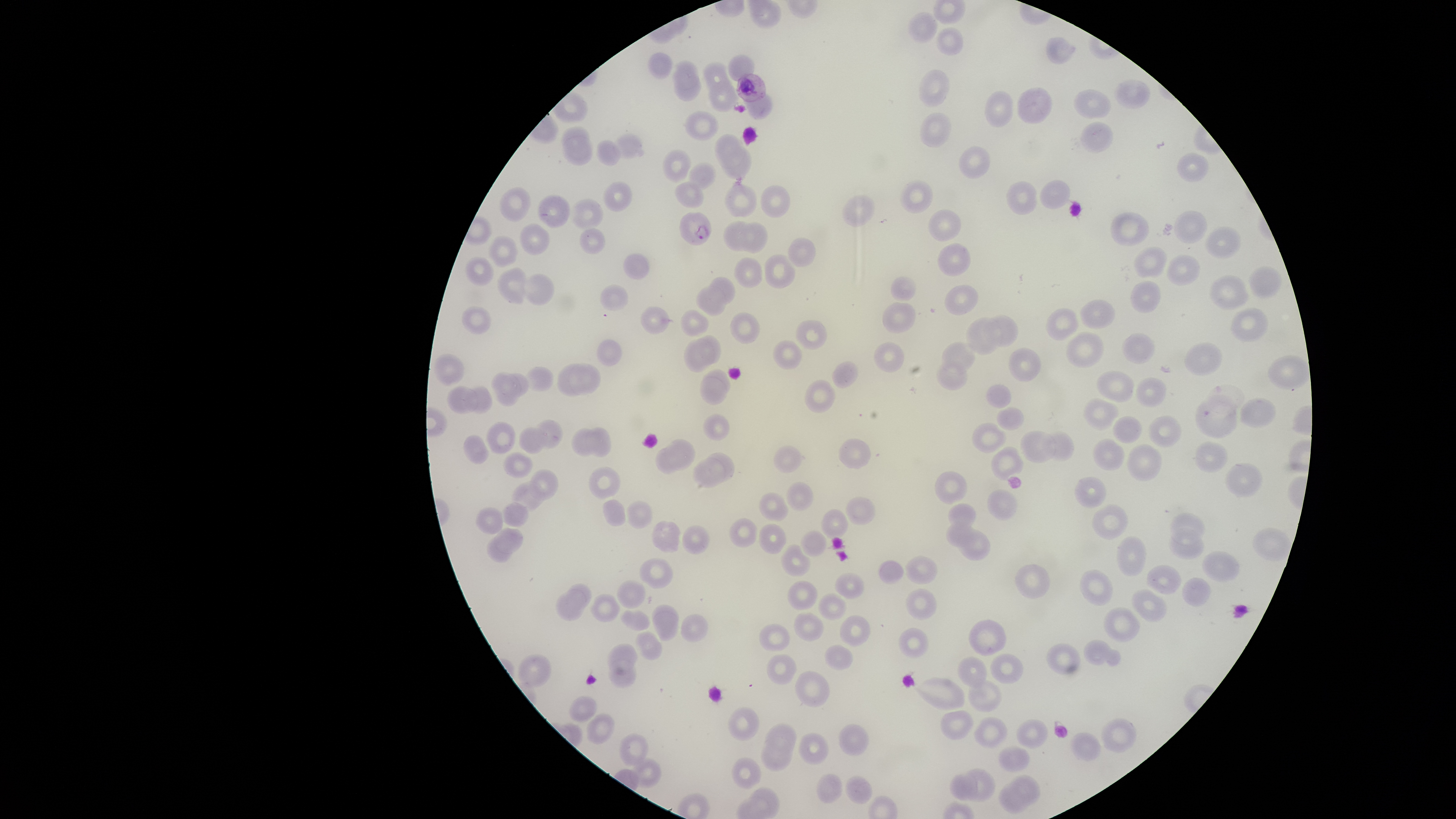
Approximate bounding boxes, in pixels from the top-left corner.
Summary:
  - Parasitized RBCs: (left=736, top=73, right=766, bottom=102), (left=679, top=211, right=712, bottom=246)
  - Uninfected RBCs: (left=747, top=0, right=782, bottom=28), (left=908, top=12, right=939, bottom=43), (left=935, top=26, right=964, bottom=55), (left=1045, top=36, right=1077, bottom=64), (left=648, top=52, right=672, bottom=80), (left=728, top=54, right=755, bottom=81), (left=672, top=59, right=702, bottom=89), (left=703, top=61, right=732, bottom=89), (left=919, top=69, right=950, bottom=109), (left=673, top=75, right=703, bottom=101), (left=707, top=80, right=740, bottom=113), (left=1113, top=80, right=1151, bottom=108), (left=1017, top=87, right=1052, bottom=124), (left=1073, top=89, right=1113, bottom=119), (left=984, top=90, right=1014, bottom=128), (left=743, top=94, right=772, bottom=120), (left=683, top=110, right=720, bottom=141), (left=920, top=112, right=952, bottom=149), (left=1080, top=121, right=1113, bottom=154), (left=562, top=125, right=588, bottom=149), (left=613, top=133, right=645, bottom=159), (left=715, top=133, right=746, bottom=166), (left=563, top=136, right=593, bottom=165), (left=596, top=139, right=621, bottom=166), (left=958, top=145, right=991, bottom=180), (left=721, top=147, right=751, bottom=181), (left=662, top=149, right=692, bottom=183), (left=1176, top=152, right=1210, bottom=182), (left=689, top=162, right=715, bottom=192), (left=899, top=180, right=934, bottom=214), (left=1006, top=180, right=1038, bottom=215), (left=1039, top=180, right=1071, bottom=210), (left=603, top=181, right=632, bottom=211), (left=675, top=181, right=704, bottom=208), (left=725, top=185, right=757, bottom=218), (left=760, top=185, right=791, bottom=218), (left=499, top=186, right=532, bottom=223), (left=536, top=195, right=570, bottom=229), (left=841, top=195, right=875, bottom=228), (left=570, top=199, right=604, bottom=230), (left=928, top=209, right=961, bottom=242), (left=1173, top=210, right=1208, bottom=245), (left=1110, top=212, right=1150, bottom=246), (left=723, top=219, right=758, bottom=252), (left=740, top=222, right=768, bottom=254), (left=520, top=223, right=550, bottom=256), (left=1205, top=226, right=1242, bottom=259), (left=580, top=228, right=605, bottom=255), (left=488, top=236, right=517, bottom=266), (left=788, top=237, right=816, bottom=268), (left=937, top=243, right=971, bottom=276), (left=1133, top=246, right=1169, bottom=278), (left=623, top=252, right=651, bottom=280), (left=763, top=253, right=795, bottom=289), (left=1165, top=255, right=1201, bottom=286), (left=465, top=256, right=495, bottom=285), (left=733, top=256, right=763, bottom=288), (left=1249, top=266, right=1282, bottom=297), (left=497, top=267, right=526, bottom=305), (left=525, top=273, right=555, bottom=306), (left=1209, top=275, right=1250, bottom=310), (left=709, top=276, right=736, bottom=305), (left=891, top=276, right=917, bottom=301), (left=1130, top=280, right=1161, bottom=314), (left=600, top=284, right=629, bottom=312), (left=944, top=285, right=978, bottom=315), (left=695, top=286, right=727, bottom=317), (left=1079, top=298, right=1116, bottom=329), (left=881, top=301, right=916, bottom=334), (left=462, top=305, right=492, bottom=334), (left=641, top=306, right=671, bottom=334), (left=1046, top=307, right=1080, bottom=341), (left=1230, top=307, right=1268, bottom=340), (left=680, top=308, right=709, bottom=338), (left=729, top=312, right=761, bottom=344), (left=983, top=314, right=1019, bottom=347), (left=965, top=316, right=1003, bottom=355), (left=795, top=320, right=828, bottom=349), (left=1066, top=331, right=1105, bottom=369), (left=1122, top=332, right=1156, bottom=364), (left=695, top=335, right=721, bottom=365), (left=596, top=339, right=623, bottom=366), (left=684, top=339, right=714, bottom=373), (left=772, top=340, right=802, bottom=369), (left=873, top=341, right=905, bottom=372), (left=942, top=342, right=975, bottom=373), (left=1184, top=342, right=1223, bottom=376), (left=1007, top=347, right=1042, bottom=382), (left=434, top=353, right=464, bottom=386), (left=831, top=360, right=859, bottom=389), (left=568, top=361, right=601, bottom=395), (left=935, top=361, right=968, bottom=390), (left=558, top=362, right=587, bottom=397), (left=525, top=366, right=554, bottom=392), (left=703, top=369, right=730, bottom=396), (left=491, top=371, right=521, bottom=406), (left=1097, top=371, right=1135, bottom=402), (left=507, top=372, right=529, bottom=396), (left=700, top=377, right=727, bottom=405), (left=1135, top=377, right=1167, bottom=407), (left=804, top=379, right=837, bottom=414), (left=987, top=384, right=1012, bottom=409), (left=447, top=385, right=479, bottom=414), (left=464, top=386, right=493, bottom=414), (left=1083, top=398, right=1120, bottom=431), (left=1240, top=398, right=1276, bottom=428), (left=1196, top=400, right=1239, bottom=439), (left=996, top=407, right=1025, bottom=431), (left=703, top=414, right=730, bottom=441), (left=1148, top=415, right=1182, bottom=448), (left=1113, top=416, right=1142, bottom=443), (left=534, top=419, right=563, bottom=448), (left=486, top=421, right=517, bottom=454), (left=972, top=421, right=1006, bottom=454), (left=518, top=426, right=547, bottom=455), (left=588, top=426, right=611, bottom=458), (left=571, top=427, right=599, bottom=457), (left=1020, top=431, right=1057, bottom=464), (left=1043, top=431, right=1075, bottom=461), (left=464, top=434, right=489, bottom=463), (left=666, top=438, right=696, bottom=470), (left=838, top=438, right=871, bottom=469), (left=1093, top=438, right=1125, bottom=471), (left=1195, top=441, right=1228, bottom=472), (left=1127, top=444, right=1162, bottom=481), (left=774, top=445, right=803, bottom=473), (left=656, top=446, right=682, bottom=475), (left=991, top=446, right=1024, bottom=481), (left=503, top=451, right=533, bottom=478), (left=704, top=453, right=735, bottom=482), (left=691, top=461, right=721, bottom=488), (left=1224, top=462, right=1263, bottom=497), (left=588, top=466, right=622, bottom=499), (left=528, top=468, right=559, bottom=500), (left=934, top=471, right=968, bottom=505), (left=1075, top=477, right=1106, bottom=509), (left=511, top=481, right=544, bottom=513), (left=786, top=482, right=814, bottom=511), (left=987, top=489, right=1018, bottom=521), (left=759, top=492, right=790, bottom=522), (left=845, top=496, right=877, bottom=525), (left=603, top=499, right=627, bottom=527), (left=626, top=500, right=654, bottom=530), (left=502, top=503, right=528, bottom=527), (left=948, top=503, right=977, bottom=530), (left=1093, top=503, right=1129, bottom=540), (left=476, top=507, right=503, bottom=535), (left=820, top=509, right=849, bottom=539), (left=1170, top=511, right=1205, bottom=546), (left=729, top=518, right=758, bottom=547), (left=652, top=520, right=683, bottom=554), (left=946, top=522, right=973, bottom=547), (left=759, top=524, right=787, bottom=554), (left=682, top=525, right=710, bottom=555), (left=1167, top=526, right=1206, bottom=560), (left=495, top=528, right=523, bottom=553), (left=957, top=528, right=991, bottom=562), (left=1252, top=528, right=1292, bottom=562), (left=800, top=530, right=827, bottom=556), (left=486, top=536, right=512, bottom=562), (left=1116, top=536, right=1146, bottom=577), (left=781, top=544, right=810, bottom=577), (left=1202, top=551, right=1239, bottom=582), (left=905, top=555, right=939, bottom=585), (left=639, top=557, right=674, bottom=590), (left=878, top=560, right=904, bottom=585), (left=1015, top=563, right=1050, bottom=599), (left=1145, top=565, right=1181, bottom=595), (left=1079, top=568, right=1113, bottom=607), (left=834, top=573, right=864, bottom=600), (left=1181, top=577, right=1212, bottom=607), (left=617, top=580, right=647, bottom=609), (left=787, top=581, right=817, bottom=609), (left=565, top=583, right=592, bottom=610), (left=906, top=588, right=938, bottom=621), (left=1132, top=589, right=1168, bottom=623), (left=556, top=592, right=584, bottom=621), (left=818, top=592, right=848, bottom=620), (left=590, top=593, right=621, bottom=623), (left=652, top=604, right=680, bottom=642), (left=1103, top=607, right=1141, bottom=644), (left=619, top=609, right=650, bottom=631), (left=794, top=611, right=825, bottom=642), (left=680, top=613, right=709, bottom=642), (left=839, top=615, right=871, bottom=648), (left=968, top=619, right=1008, bottom=657), (left=758, top=623, right=790, bottom=652), (left=898, top=628, right=929, bottom=659), (left=635, top=630, right=663, bottom=661), (left=1084, top=639, right=1121, bottom=666), (left=1047, top=642, right=1081, bottom=674), (left=607, top=643, right=637, bottom=674), (left=825, top=644, right=853, bottom=670), (left=990, top=653, right=1024, bottom=685), (left=517, top=654, right=551, bottom=689), (left=766, top=654, right=798, bottom=685), (left=957, top=657, right=988, bottom=689), (left=609, top=660, right=637, bottom=689), (left=794, top=670, right=830, bottom=708), (left=914, top=677, right=965, bottom=711), (left=967, top=679, right=1001, bottom=714), (left=569, top=695, right=597, bottom=722), (left=728, top=706, right=760, bottom=741), (left=940, top=710, right=975, bottom=741), (left=586, top=713, right=614, bottom=744), (left=973, top=717, right=1009, bottom=750), (left=1102, top=718, right=1137, bottom=753), (left=1016, top=719, right=1049, bottom=749), (left=764, top=723, right=797, bottom=754), (left=838, top=724, right=869, bottom=757), (left=620, top=733, right=647, bottom=766), (left=798, top=733, right=828, bottom=765), (left=1071, top=733, right=1101, bottom=762), (left=761, top=738, right=793, bottom=771), (left=998, top=746, right=1030, bottom=772), (left=631, top=757, right=661, bottom=788), (left=732, top=757, right=761, bottom=790), (left=962, top=769, right=995, bottom=802), (left=816, top=773, right=843, bottom=804), (left=949, top=773, right=978, bottom=800), (left=845, top=775, right=873, bottom=804), (left=1010, top=776, right=1039, bottom=805), (left=999, top=783, right=1030, bottom=815), (left=750, top=788, right=779, bottom=816)
  - Image size: 1456×819 pixels
  - Presence: malaria parasites detected
  - Field of view: single
  - Stain: Giemsa
  - Visible region: circular
  - Species: Plasmodium falciparum
  - Preparation: thin smear of blood
  - Capture: smartphone photograph through the microscope eyepiece